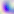
Summary:
  - Identification: Toxoplasma gondii
  - Magnification: 400x
  - Modality: photomicrograph